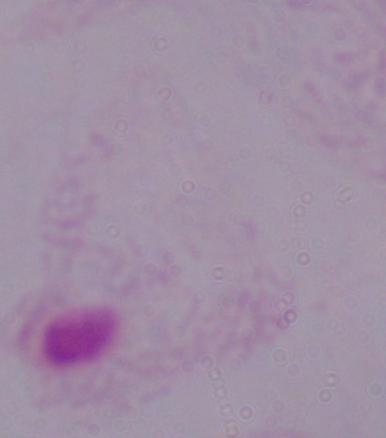

{
  "modality": "micrograph",
  "identification": "trichomonad",
  "magnification": "1000x"
}